Name the cell type shown.
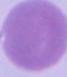
An erythrocyte.

Summary:
  - Magnification: 1000x
  - Modality: photomicrograph